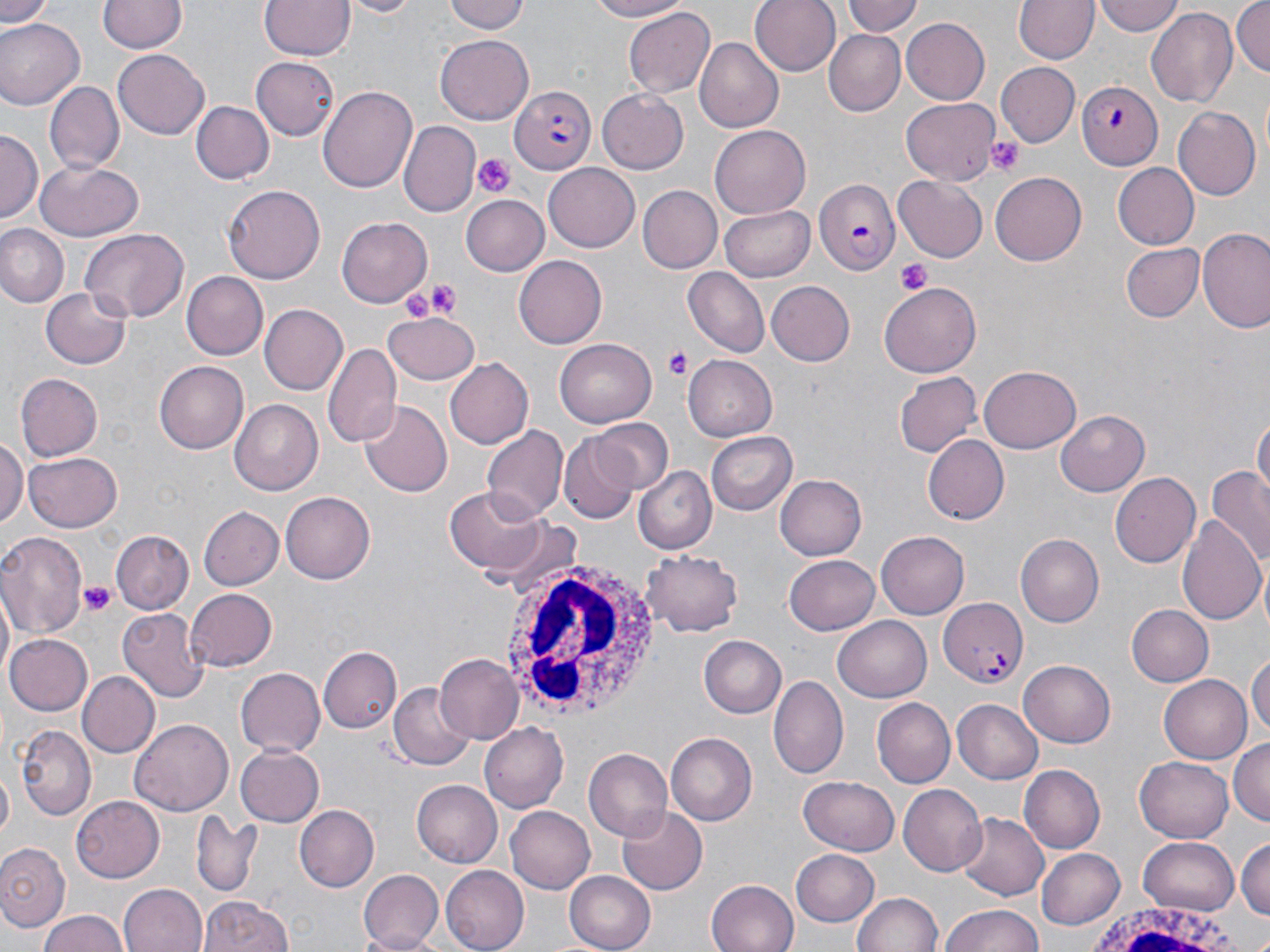
Approximate bounding boxes as (x1, y1, x2, y2) in pixels. Platelet locations: (988, 135, 1024, 176), (471, 152, 517, 198), (894, 258, 935, 295), (425, 279, 461, 318), (399, 284, 443, 324), (666, 347, 693, 381), (82, 582, 115, 617). White blood cell locations: (502, 558, 662, 721), (1084, 903, 1246, 952). Uninfected red blood cell locations: (0, 0, 54, 26), (100, 0, 184, 54), (259, 0, 354, 61), (337, 0, 420, 17), (446, 0, 528, 35), (583, 0, 688, 23), (751, 0, 841, 76), (842, 0, 922, 40), (1014, 0, 1098, 65), (1096, 0, 1184, 37), (1231, 0, 1269, 80), (1179, 3, 1267, 100), (439, 5, 530, 75), (625, 7, 715, 99), (1147, 8, 1237, 109), (899, 16, 989, 103), (0, 17, 82, 108), (822, 28, 907, 116), (437, 36, 533, 123), (693, 39, 782, 132), (112, 50, 209, 141), (252, 57, 339, 139), (995, 62, 1081, 147), (45, 79, 124, 175), (319, 84, 416, 194), (598, 90, 689, 172), (901, 99, 998, 184), (191, 101, 271, 182), (1171, 106, 1260, 202), (397, 121, 480, 217), (710, 127, 810, 214), (0, 130, 41, 220), (35, 161, 143, 242), (543, 163, 641, 252), (1111, 164, 1197, 250), (990, 170, 1087, 263), (893, 175, 988, 261), (222, 184, 326, 283), (637, 184, 722, 272), (461, 193, 548, 274), (721, 204, 816, 280), (338, 218, 431, 305), (0, 224, 68, 306), (79, 228, 188, 322), (1199, 230, 1270, 334), (1121, 242, 1205, 323), (514, 256, 607, 348), (682, 267, 769, 355), (180, 271, 269, 359), (767, 279, 855, 365), (879, 283, 980, 379), (42, 287, 131, 369), (260, 304, 349, 394), (385, 311, 481, 386), (555, 338, 657, 426), (323, 342, 402, 448), (683, 355, 778, 440), (444, 358, 532, 451), (153, 361, 246, 454), (981, 365, 1082, 454), (895, 371, 984, 458), (15, 373, 102, 461), (230, 400, 324, 494), (359, 400, 452, 497), (1055, 410, 1150, 497), (1253, 413, 1269, 505), (588, 417, 674, 494), (482, 422, 567, 523), (706, 431, 797, 515), (558, 434, 638, 523), (923, 435, 1009, 524), (0, 439, 26, 529), (25, 448, 123, 531), (632, 464, 717, 553), (1206, 468, 1270, 566), (1111, 472, 1200, 568), (774, 474, 867, 562), (448, 486, 549, 572), (279, 491, 373, 583), (203, 508, 283, 592), (1178, 513, 1265, 626), (0, 530, 86, 640), (111, 530, 193, 615), (875, 532, 970, 618), (1014, 533, 1103, 627), (639, 550, 743, 637), (783, 553, 879, 634), (1, 585, 15, 683), (183, 588, 277, 670), (1124, 604, 1213, 687), (118, 609, 208, 703), (834, 617, 931, 702), (3, 634, 92, 716), (698, 635, 785, 718), (319, 647, 401, 732), (1249, 649, 1269, 746), (435, 654, 524, 742), (1019, 661, 1116, 746), (233, 668, 325, 757), (77, 670, 160, 758), (1160, 672, 1255, 763), (768, 674, 847, 779), (389, 686, 473, 770), (871, 698, 955, 788), (952, 699, 1045, 784), (133, 719, 233, 813), (479, 723, 567, 813), (16, 725, 96, 819), (666, 733, 756, 825), (1229, 736, 1270, 823), (235, 744, 323, 826), (582, 746, 673, 841), (1136, 755, 1235, 843), (1020, 766, 1104, 852), (797, 777, 899, 855), (411, 781, 502, 868), (899, 784, 987, 876), (71, 796, 164, 883), (297, 805, 379, 892), (504, 805, 595, 895), (615, 806, 707, 896), (193, 814, 263, 895), (957, 814, 1049, 902), (1140, 835, 1241, 915), (1236, 836, 1269, 921), (0, 844, 70, 932), (1035, 846, 1126, 930), (790, 848, 879, 926), (440, 866, 527, 952), (358, 869, 445, 951), (564, 870, 655, 952), (706, 879, 801, 952), (119, 883, 209, 952), (852, 891, 945, 952), (197, 894, 293, 952), (938, 904, 1047, 952), (35, 911, 132, 952). Plasmodium falciparum-infected red blood cell locations: (1075, 82, 1163, 169), (512, 84, 595, 174), (813, 176, 900, 274), (940, 598, 1029, 687). Slide-level diagnosis: Plasmodium falciparum. May-Grünwald-Giemsa stain. Image is 1270×952 pixels. Captured at 1000x magnification. Thin blood smear. Single field of view. Light microscopy.